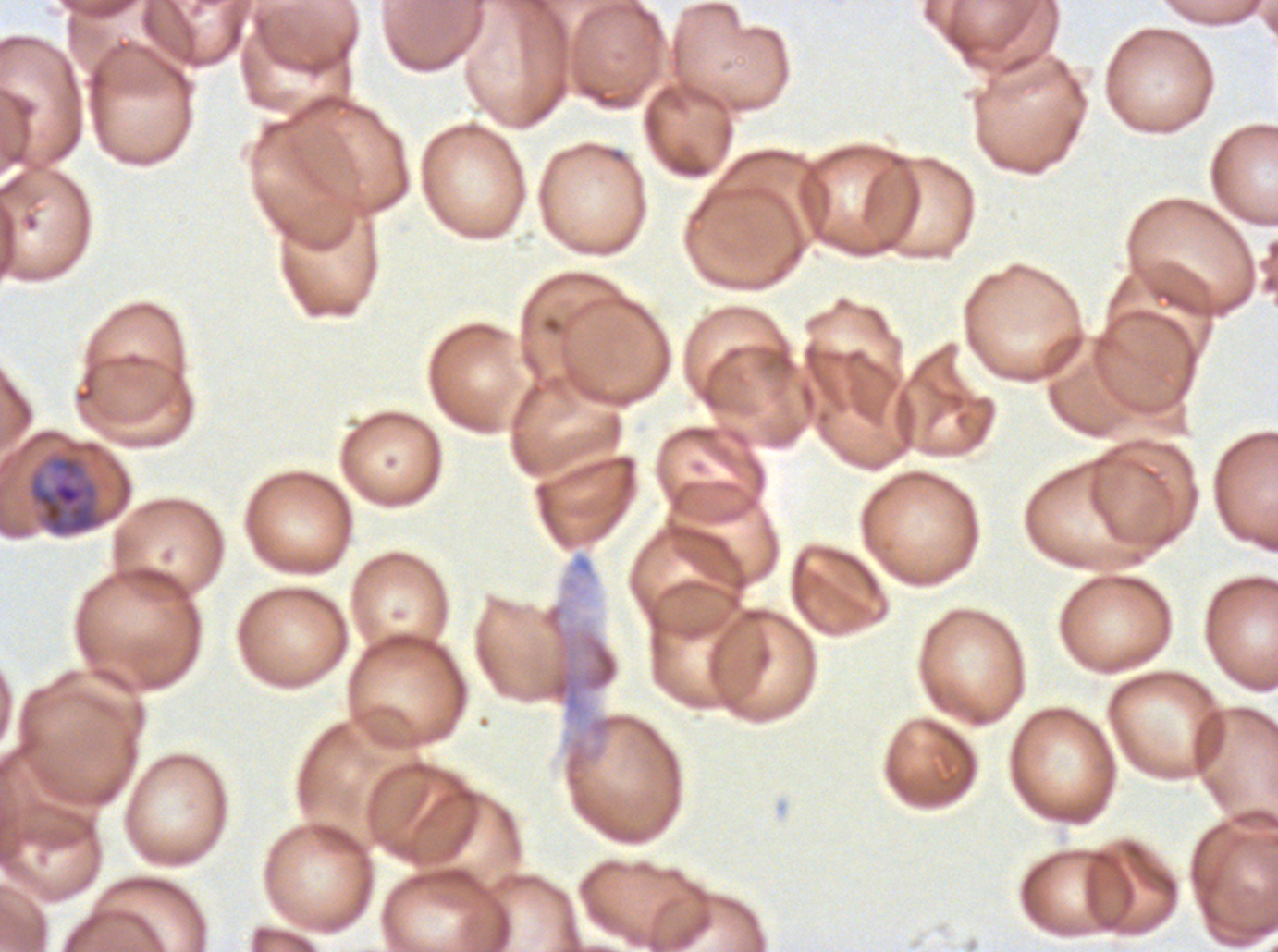
Approximate bounding boxes as (x1, y1, x2, y2) in pixels.
Summary:
  - Late trophozoite locations: (28, 454, 107, 537)
  - Stain: Giemsa
  - Preparation: thin blood film
  - Image size: 1278×952 pixels
  - Field of view: one sub-image of a larger composite
  - Specimen: P. falciparum from a patient in The Gambia, cultured ex vivo for 24 to 48 hours